Describe the morphology of the erythrocytes.
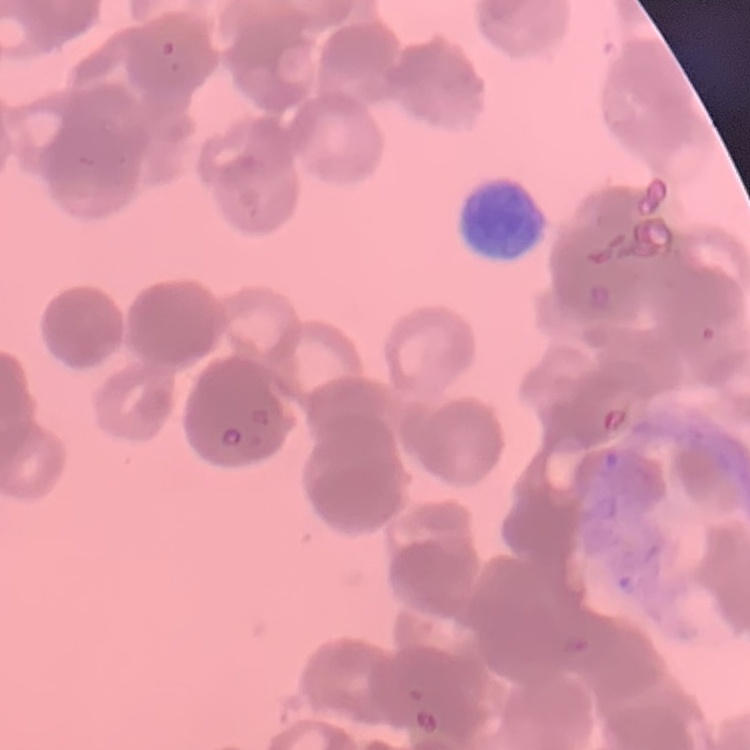
They show rouleaux formation.

Summary:
  - Preparation: thin peripheral smear
  - Stain: Field's or Giemsa
  - Image type: square crop of a larger photomicrograph